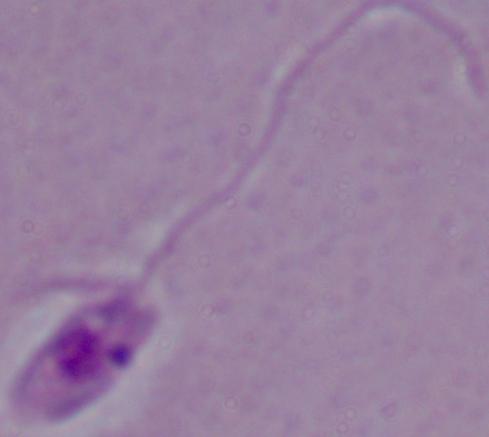
Summary:
  - Modality: micrograph
  - Magnification: 1000x
  - Identification: Leishmania